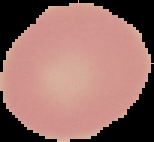
Cell region segmented out of the field of view; the surrounding area is masked to black. Image is 154×142 pixels. Malaria status: uninfected. From a thin blood smear.